Classify this cell by malaria status.
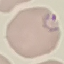

Parasitized.

Summary:
  - Preparation: thin smear
  - Stain: Giemsa
  - Image type: cell patch, automatically extracted from a larger field of view and resized to 64 × 64 pixels
  - Capture: smartphone camera at the microscope eyepiece